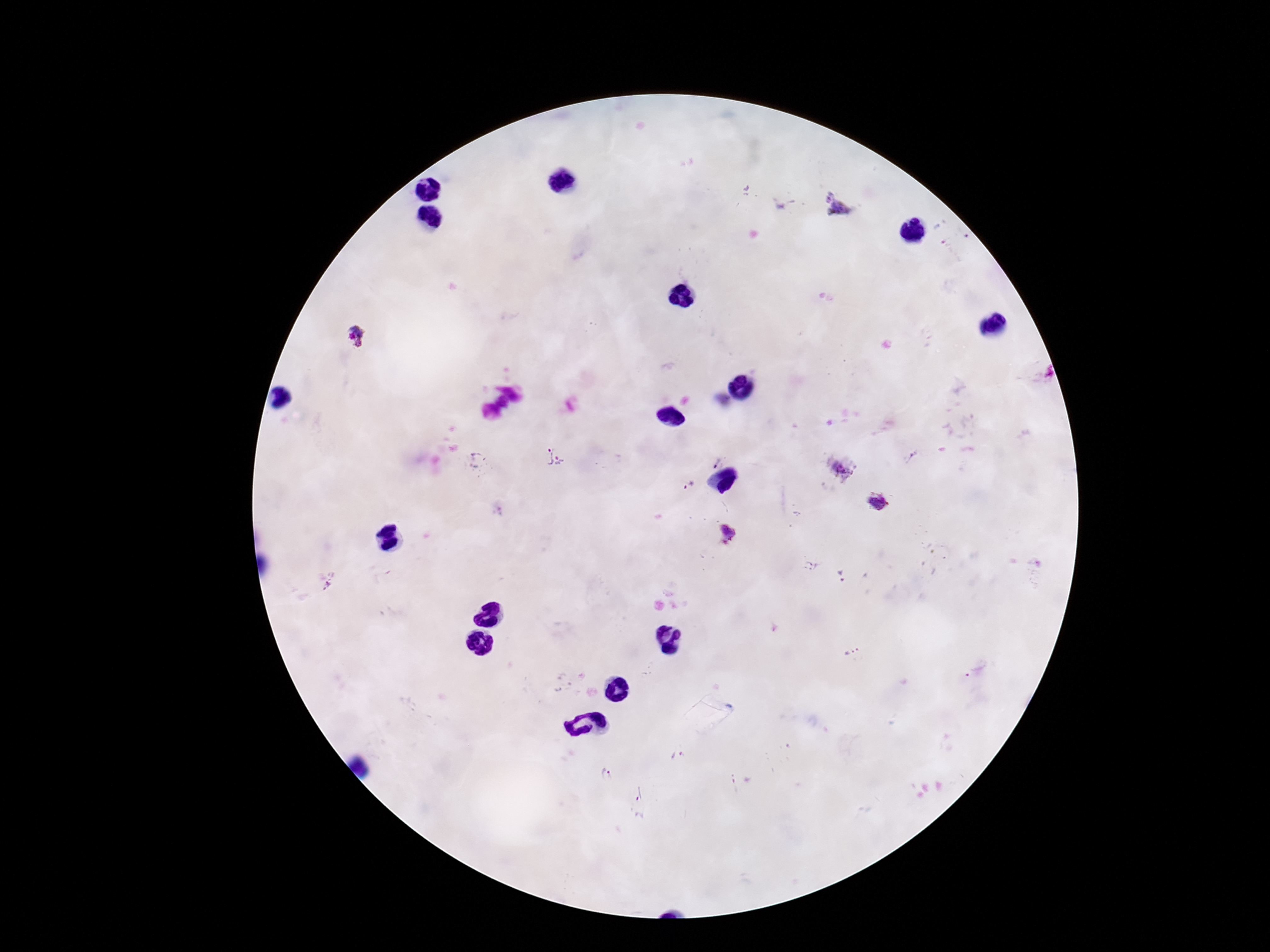
Approximate centers as [x, y] in pixels. Plasmodium parasite locations: [837, 204], [354, 336], [476, 455], [545, 456], [711, 460], [560, 461], [838, 469], [689, 484], [877, 501], [727, 534], [811, 566], [841, 575], [851, 651], [677, 757], [606, 775], [734, 777], [638, 793]. One field from this slide. Patient malaria status: infected. Image is 1270×952 pixels. Giemsa-stained preparation. Photographed through the microscope eyepiece with a smartphone camera. 100x magnification. Thick peripheral-blood smear.